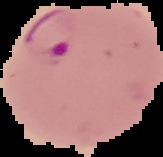

Summary:
  - Malaria status: parasitized
  - Preparation: thin blood film
  - Image size: 163×157 pixels
  - Image type: segmented cell region on a black background